Outline each blood parasite and name the species.
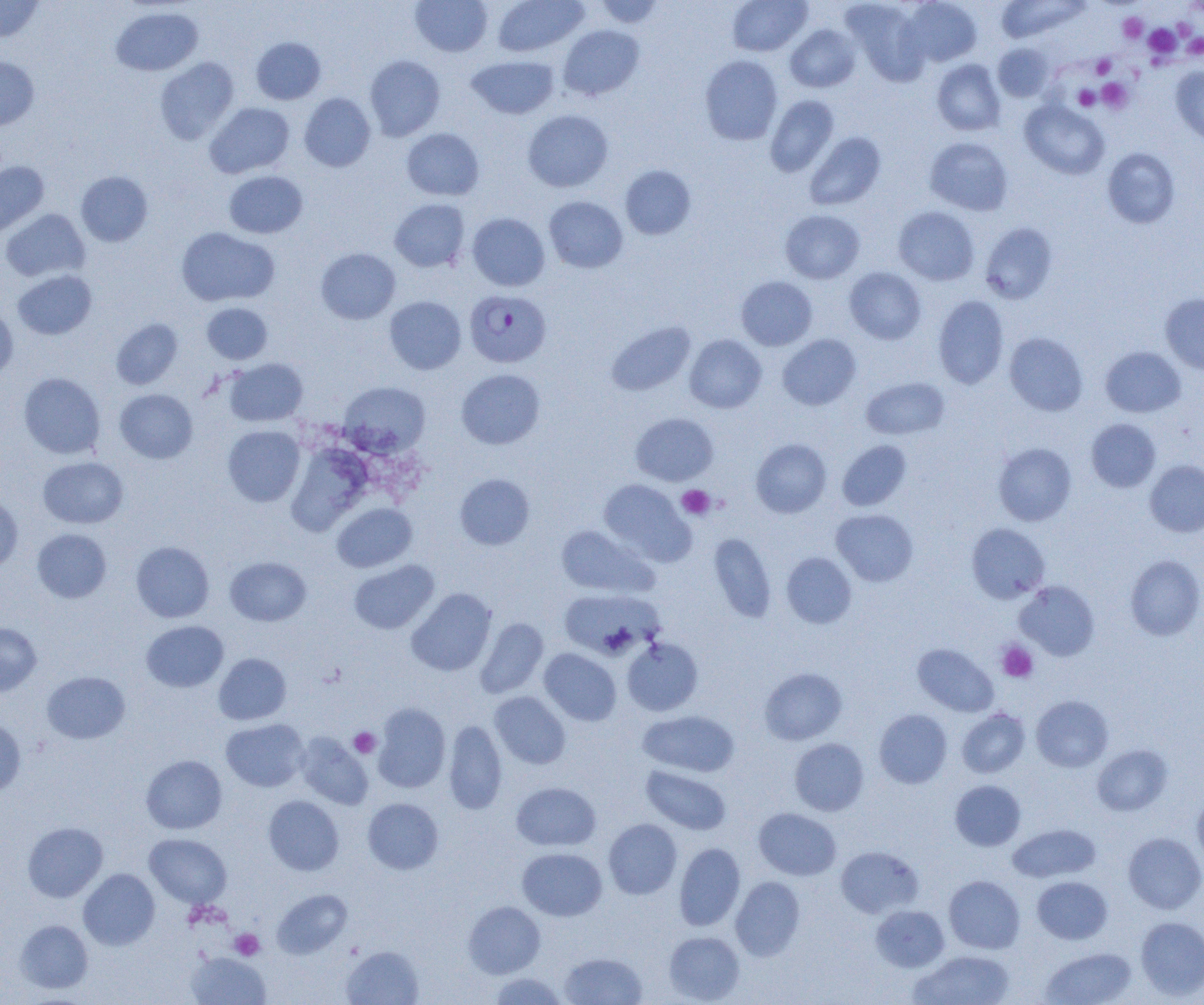

Approximate bounding boxes as [x1, y1, x2, y2] in pixels.
Plasmodium falciparum-infected red blood cells: [465, 289, 551, 368].
No Plasmodium ovale, Plasmodium malariae, Plasmodium vivax, Babesia divergens, or Trypanosoma brucei observed.

{
  "slide_level_diagnosis": "Plasmodium falciparum",
  "field_of_view": "one of a larger specimen",
  "magnification": "1000x",
  "modality": "light microscopy",
  "preparation": "thin blood film",
  "uninfected_red_blood_cell_locations": "approximate bounding boxes as [x1, y1, x2, y2] in pixels: [0, 0, 45, 42], [410, 0, 493, 57], [493, 0, 588, 57], [594, 0, 666, 28], [727, 0, 812, 56], [901, 0, 982, 67], [842, 1, 930, 84], [996, 1, 1087, 43], [110, 6, 203, 76], [785, 24, 861, 92], [558, 25, 644, 100], [251, 37, 326, 104], [993, 43, 1054, 102], [364, 55, 445, 141], [466, 55, 559, 119], [700, 55, 783, 145], [0, 57, 39, 130], [154, 57, 239, 144], [932, 59, 1005, 136], [1171, 66, 1204, 145], [299, 93, 375, 172], [765, 95, 839, 177], [1020, 100, 1109, 179], [205, 102, 295, 178], [523, 110, 613, 192], [402, 128, 484, 200], [804, 132, 886, 210], [925, 137, 1013, 216], [1102, 148, 1180, 229], [0, 161, 50, 238], [620, 165, 696, 239], [76, 171, 153, 247], [224, 171, 308, 238], [544, 196, 628, 273], [389, 198, 470, 272], [893, 206, 979, 285], [1, 209, 90, 282], [780, 210, 864, 284], [468, 212, 550, 291], [980, 223, 1058, 304], [176, 227, 279, 306], [316, 248, 400, 324], [844, 267, 926, 344], [12, 270, 97, 339], [736, 276, 817, 350], [1160, 293, 1204, 374], [933, 295, 1009, 389], [384, 296, 466, 374], [202, 302, 273, 364], [0, 303, 18, 383], [111, 318, 183, 390], [606, 321, 696, 396], [1004, 332, 1088, 415], [685, 334, 766, 413], [777, 334, 861, 410], [1100, 347, 1186, 417], [224, 358, 308, 427], [456, 369, 545, 449], [18, 372, 105, 459], [861, 377, 950, 440], [340, 381, 430, 456], [115, 389, 198, 463], [630, 412, 718, 486], [1086, 419, 1161, 492], [223, 425, 305, 507], [751, 438, 832, 518], [837, 440, 912, 511], [993, 442, 1076, 526], [38, 456, 128, 528], [1145, 459, 1204, 537], [454, 473, 535, 550], [599, 480, 694, 565], [0, 492, 23, 571], [332, 503, 417, 572], [831, 509, 918, 586], [966, 523, 1050, 603], [555, 524, 658, 598], [32, 528, 111, 603], [707, 534, 776, 622], [131, 541, 214, 622], [782, 552, 856, 628], [1124, 554, 1204, 640], [225, 556, 311, 626], [349, 560, 439, 634], [1014, 580, 1100, 660], [406, 588, 496, 676], [557, 588, 662, 660], [475, 617, 548, 698], [141, 620, 228, 692], [0, 623, 41, 696], [622, 637, 703, 716], [913, 643, 999, 717], [539, 648, 621, 725], [214, 653, 291, 725], [759, 667, 847, 745], [42, 671, 130, 744], [489, 691, 570, 768], [1031, 695, 1113, 772], [372, 703, 451, 792], [957, 708, 1030, 778], [874, 709, 952, 789], [638, 710, 740, 777], [0, 717, 26, 796], [221, 718, 308, 792], [443, 720, 507, 814], [294, 732, 373, 810], [789, 738, 869, 816], [1092, 744, 1172, 816], [141, 755, 227, 834], [641, 765, 731, 835], [950, 780, 1026, 851], [511, 782, 601, 851], [1193, 792, 1204, 871], [263, 795, 344, 875], [363, 798, 444, 874], [754, 808, 841, 880], [603, 818, 682, 899], [22, 822, 108, 902], [1008, 824, 1101, 883], [1123, 832, 1204, 914], [145, 833, 232, 908], [674, 843, 745, 930], [835, 846, 923, 918], [517, 847, 607, 921], [78, 868, 160, 950], [944, 875, 1025, 953], [730, 876, 805, 961], [1032, 876, 1113, 944], [272, 889, 353, 958], [463, 901, 545, 978], [870, 905, 950, 972], [1136, 917, 1204, 1000], [16, 920, 93, 993], [663, 931, 745, 1003], [340, 945, 424, 1005], [1040, 947, 1136, 1005], [911, 950, 1015, 1005], [186, 951, 271, 1005], [559, 952, 647, 1005], [487, 972, 568, 1004]",
  "platelet_locations": "approximate bounding boxes as [x1, y1, x2, y2] in pixels: [1118, 13, 1147, 43], [1144, 24, 1181, 58], [1182, 35, 1204, 59], [1091, 54, 1116, 78], [1097, 77, 1133, 113], [1074, 85, 1099, 111], [677, 485, 715, 519], [997, 640, 1038, 682], [349, 727, 380, 758], [230, 928, 264, 959]",
  "image_size": "1204×1005 pixels"
}